Assess this cell for malaria.
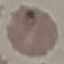
Parasitized.

Summary:
  - Image type: cell patch, automatically extracted from a larger field of view and resized to 64 × 64 pixels
  - Capture: smartphone camera at the microscope eyepiece
  - Preparation: thin blood smear
  - Stain: Giemsa